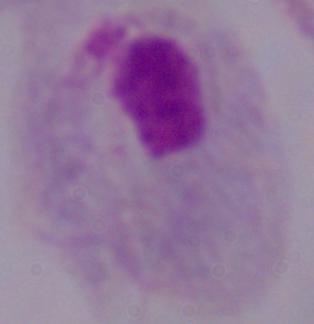
A trichomonad is shown. Photomicrograph. Captured at 1000x magnification.